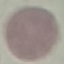

result = no malaria parasites seen
image type = cell patch, automatically extracted from a larger field of view and resized to 64 × 64 pixels
stain = Giemsa
capture = smartphone through the microscope eyepiece
preparation = thin blood smear